Report the malaria status of this cell.
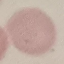

It is uninfected.

{
  "image_type": "cell patch, automatically extracted from a larger field of view and resized to 64 × 64 pixels",
  "stain": "Giemsa",
  "capture": "smartphone through the microscope eyepiece",
  "preparation": "thin smear"
}